Report the malaria status of this cell.
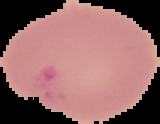
Parasitized.

{
  "preparation": "thin blood film",
  "image_size": "160×124 pixels",
  "image_type": "cell region segmented out of the field of view; surrounding area masked to black"
}